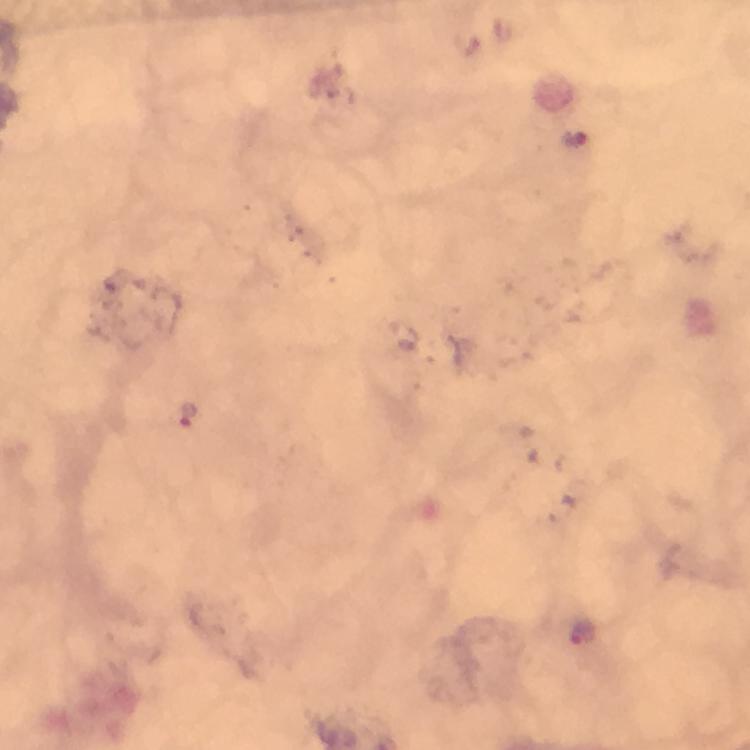

Plasmodium parasite locations = approximate object centers, in pixels from the top-left corner: (x=188, y=417), (x=584, y=633)
immersion oil = used
capture = smartphone photograph through a microscope
stain = Giemsa
context = from a malaria diagnostic workup
magnification = 100x
preparation = thick blood film
image size = 750×750 pixels
cropped from = one field of view